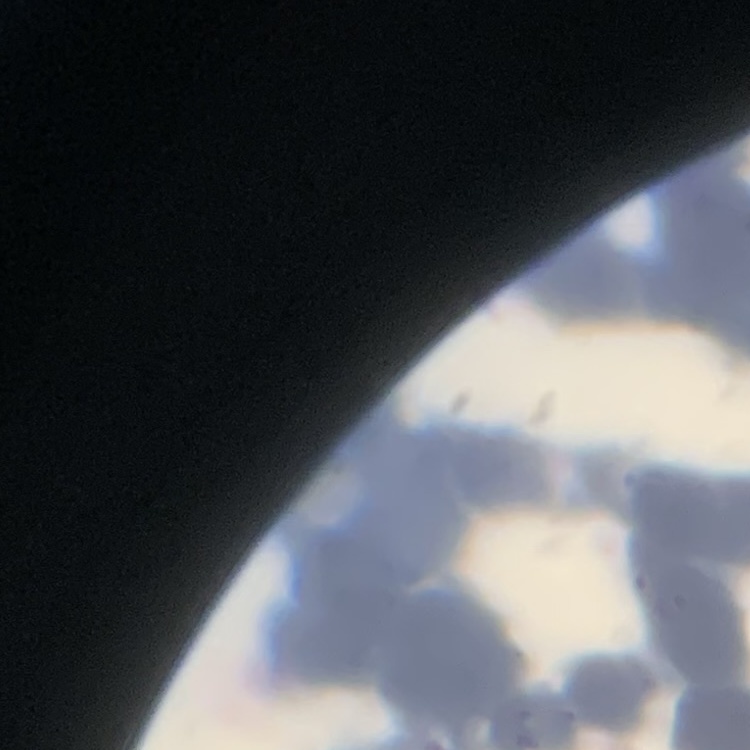

erythrocyte morphology = rouleaux formation
preparation = thin peripheral smear
stain = Field's or Giemsa
image type = square crop of a larger photomicrograph